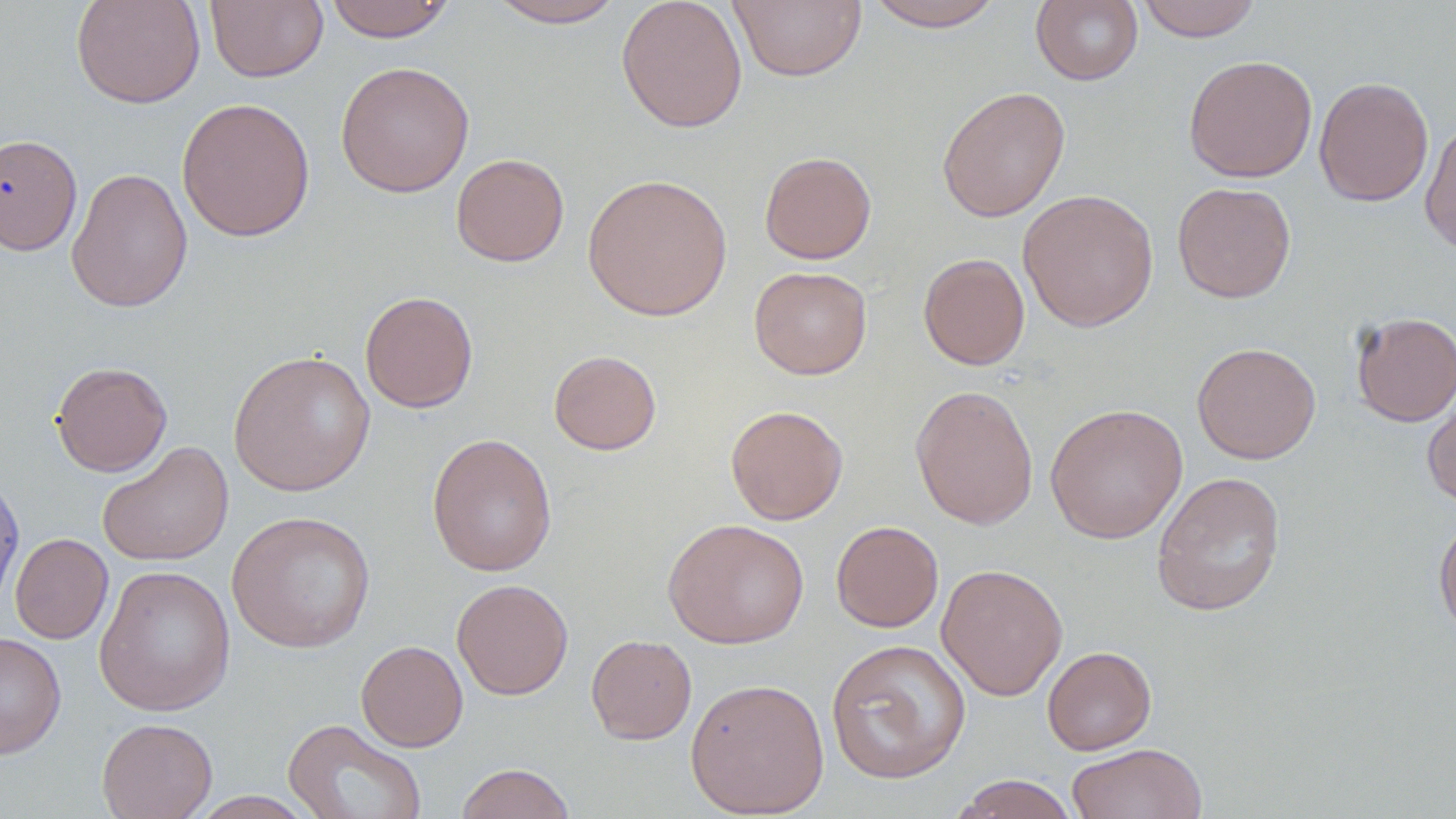

{
  "slide_level_diagnosis": "negative for blood parasites",
  "uninfected_red_blood_cell_locations": "approximate bounding boxes as (x1, y1, x2, y2) in pixels: (70, 0, 206, 109), (205, 0, 328, 83), (323, 0, 456, 42), (486, 0, 626, 28), (616, 0, 747, 133), (729, 0, 867, 83), (862, 0, 1007, 31), (1031, 0, 1144, 86), (1135, 0, 1263, 42), (1183, 54, 1318, 182), (335, 60, 474, 198), (1314, 75, 1434, 207), (936, 85, 1070, 222), (176, 96, 315, 242), (1420, 118, 1456, 257), (0, 133, 83, 256), (759, 151, 877, 264), (451, 153, 569, 266), (65, 166, 194, 313), (582, 172, 734, 322), (1171, 182, 1296, 303), (1018, 188, 1159, 332), (918, 252, 1030, 370), (749, 266, 872, 379), (359, 291, 478, 413), (1350, 312, 1456, 426), (1191, 341, 1321, 464), (228, 350, 376, 497), (549, 350, 662, 455), (50, 360, 172, 477), (910, 384, 1039, 530), (1422, 384, 1456, 510), (1045, 403, 1188, 544), (725, 405, 849, 525), (426, 432, 558, 576), (97, 440, 234, 566), (1151, 470, 1286, 617), (0, 472, 25, 614), (227, 510, 376, 653), (1433, 514, 1456, 640), (662, 517, 810, 648), (831, 521, 944, 633), (10, 533, 113, 644), (936, 563, 1068, 701), (94, 564, 236, 717), (451, 578, 574, 700), (0, 632, 67, 759), (585, 634, 697, 745), (356, 639, 468, 752), (825, 639, 971, 784), (1042, 645, 1157, 755), (685, 677, 830, 818), (97, 717, 218, 819), (283, 718, 427, 819), (1067, 743, 1208, 819), (454, 763, 577, 819), (948, 774, 1081, 819), (188, 791, 319, 819)",
  "preparation": "thin blood smear",
  "image_size": "1456×819 pixels",
  "modality": "optical microscopy",
  "field_of_view": "single",
  "stain": "May-Grünwald-Giemsa",
  "magnification": "1000x"
}